Comment on the morphology of the erythrocytes.
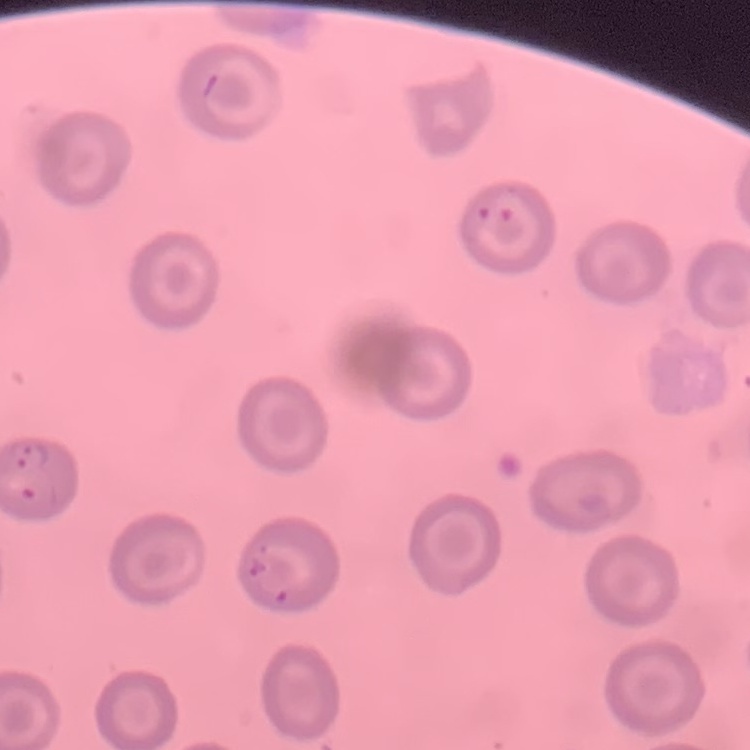

No rouleaux formation.

Stained with either Field's or Giemsa. Thin blood smear. One tile cut from a larger photomicrograph.